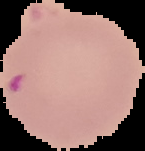 Result: malaria parasites detected. Cell region segmented out of the field of view; the surrounding area is masked to black. Image is 145×151 pixels. From a thin blood smear.